Point out each Plasmodium parasite.
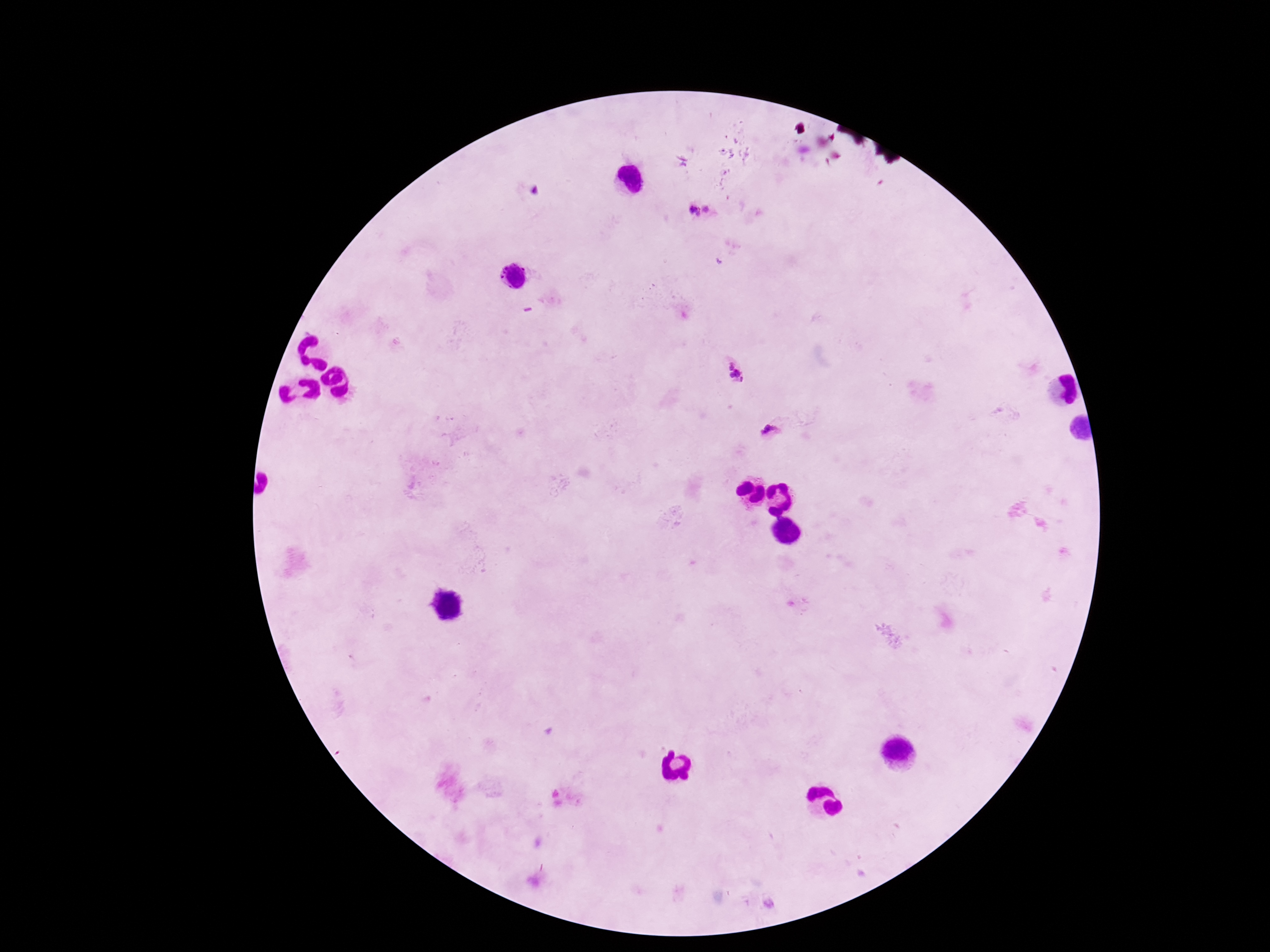
Approximate object centers, in pixels from the top-left corner.
Plasmodium parasites: (x=701, y=214), (x=739, y=376), (x=774, y=431).

Summary:
  - Preparation: thick blood smear
  - Patient malaria status: infected
  - Image size: 1270×952 pixels
  - Field of view: single
  - Magnification: 100x
  - Stain: Giemsa
  - Capture: smartphone camera through the microscope eyepiece